Assess this cell for malaria.
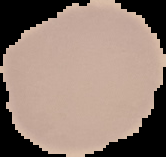

Uninfected.

{
  "preparation": "thin blood film",
  "image_size": "166×157 pixels",
  "image_type": "cell region segmented out of the field of view; surrounding area masked to black"
}